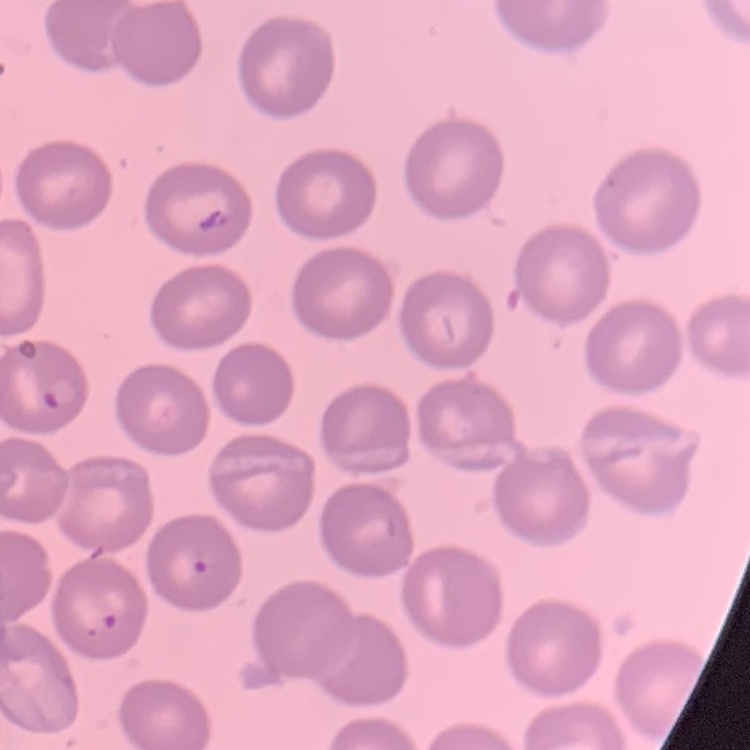

red blood cell morphology = no rouleaux formation
stain = Field's or Giemsa
image type = one tile cut from a larger photomicrograph
preparation = thin peripheral smear